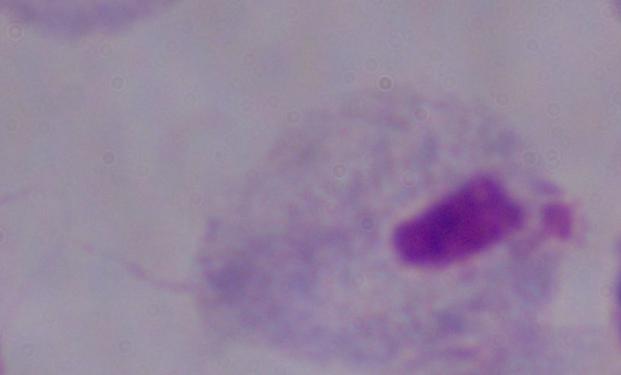

Summary:
  - Modality: micrograph
  - Magnification: 1000x
  - Identification: trichomonad